Mark where platelets are.
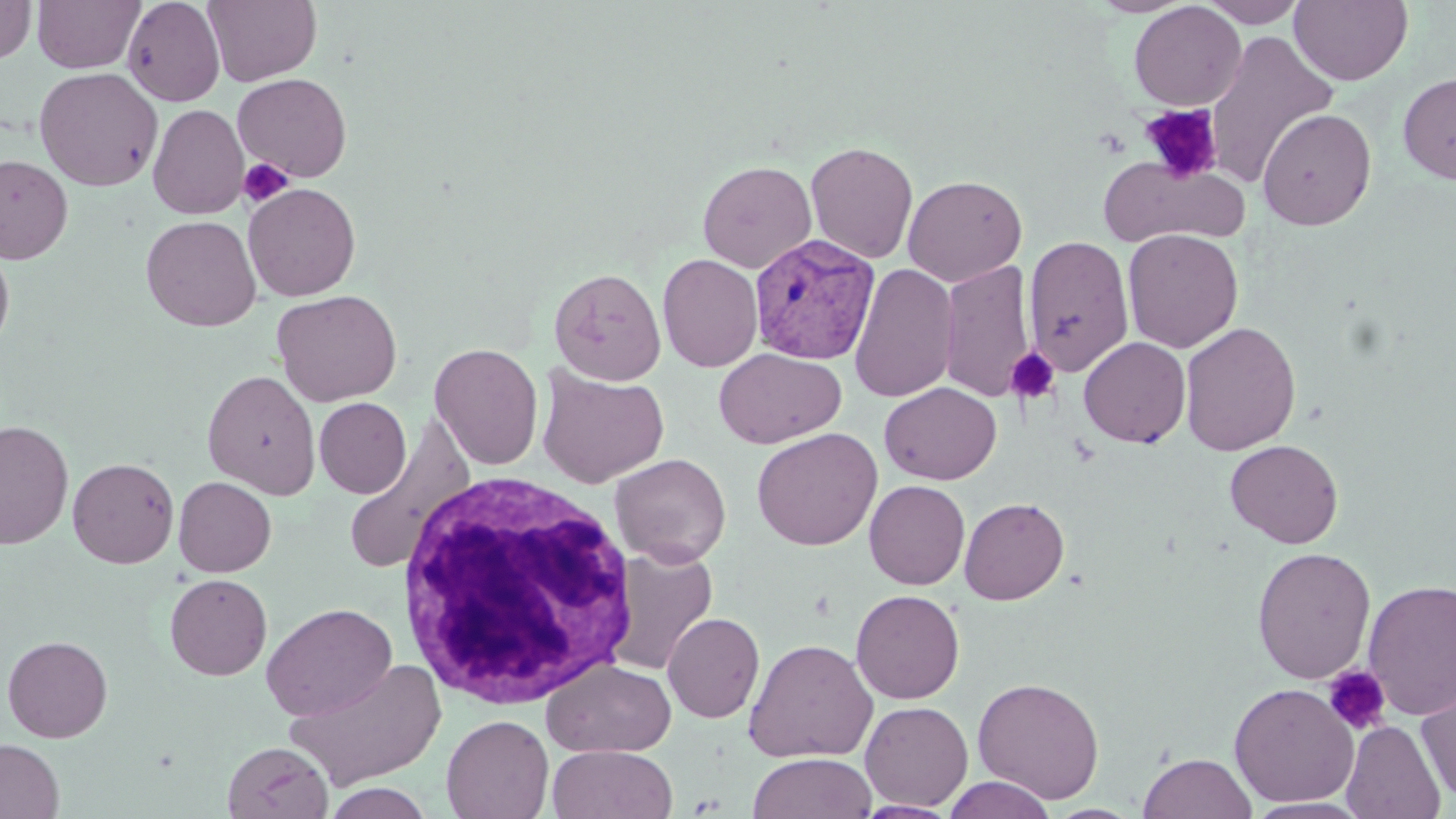
Approximate bounding boxes as [x1, y1, x2, y2] in pixels.
Platelets: [1139, 104, 1223, 184], [238, 157, 294, 207], [1006, 347, 1061, 406], [1323, 665, 1392, 736].

Summary:
  - White blood cell locations: [397, 471, 642, 708]
  - Uninfected red blood cell locations: [32, 0, 144, 73], [123, 0, 225, 106], [203, 0, 322, 86], [1090, 0, 1196, 17], [1199, 0, 1309, 27], [1289, 0, 1413, 86], [0, 1, 36, 64], [1129, 1, 1246, 111], [1203, 29, 1337, 188], [34, 66, 163, 192], [1398, 71, 1456, 185], [233, 72, 352, 181], [148, 104, 248, 219], [1257, 108, 1377, 230], [805, 140, 919, 264], [1099, 154, 1250, 250], [0, 155, 73, 263], [698, 160, 817, 272], [903, 174, 1027, 286], [243, 182, 361, 301], [141, 215, 261, 332], [1122, 228, 1243, 353], [1023, 235, 1134, 376], [0, 241, 15, 360], [657, 253, 763, 372], [940, 261, 1035, 403], [849, 263, 959, 403], [549, 267, 666, 384], [271, 289, 402, 407], [1179, 321, 1301, 456], [1079, 336, 1191, 448], [429, 342, 544, 470], [713, 347, 846, 448], [536, 366, 669, 488], [202, 369, 321, 499], [879, 382, 1002, 485], [314, 397, 411, 499], [341, 418, 475, 576], [1, 419, 74, 549], [751, 427, 883, 551], [1225, 439, 1343, 548], [610, 452, 731, 567], [67, 457, 179, 568], [173, 476, 276, 577], [864, 480, 970, 590], [959, 497, 1069, 604], [605, 546, 719, 677], [1251, 547, 1376, 684], [164, 573, 272, 681], [1362, 578, 1456, 720], [851, 589, 965, 704], [261, 602, 398, 721], [662, 612, 765, 723], [2, 634, 113, 742], [743, 638, 878, 763], [284, 658, 447, 791], [541, 660, 677, 757], [1416, 675, 1456, 806], [972, 676, 1105, 803], [1229, 683, 1359, 807], [859, 700, 974, 810], [441, 714, 553, 818], [1341, 719, 1445, 819], [0, 738, 64, 819], [222, 741, 333, 819], [547, 745, 678, 819], [748, 752, 876, 819], [1138, 752, 1256, 819], [941, 776, 1057, 819], [323, 782, 434, 819], [1244, 798, 1372, 818], [853, 800, 961, 819]
  - Plasmodium vivax-infected red blood cell locations: [748, 233, 880, 363]
  - Slide-level diagnosis: Plasmodium vivax
  - Field of view: single
  - Stain: May-Grünwald-Giemsa
  - Image size: 1456×819 pixels
  - Modality: optical microscopy
  - Magnification: 1000x
  - Preparation: thin blood film